Outline malaria parasites and classify them by life-cycle stage.
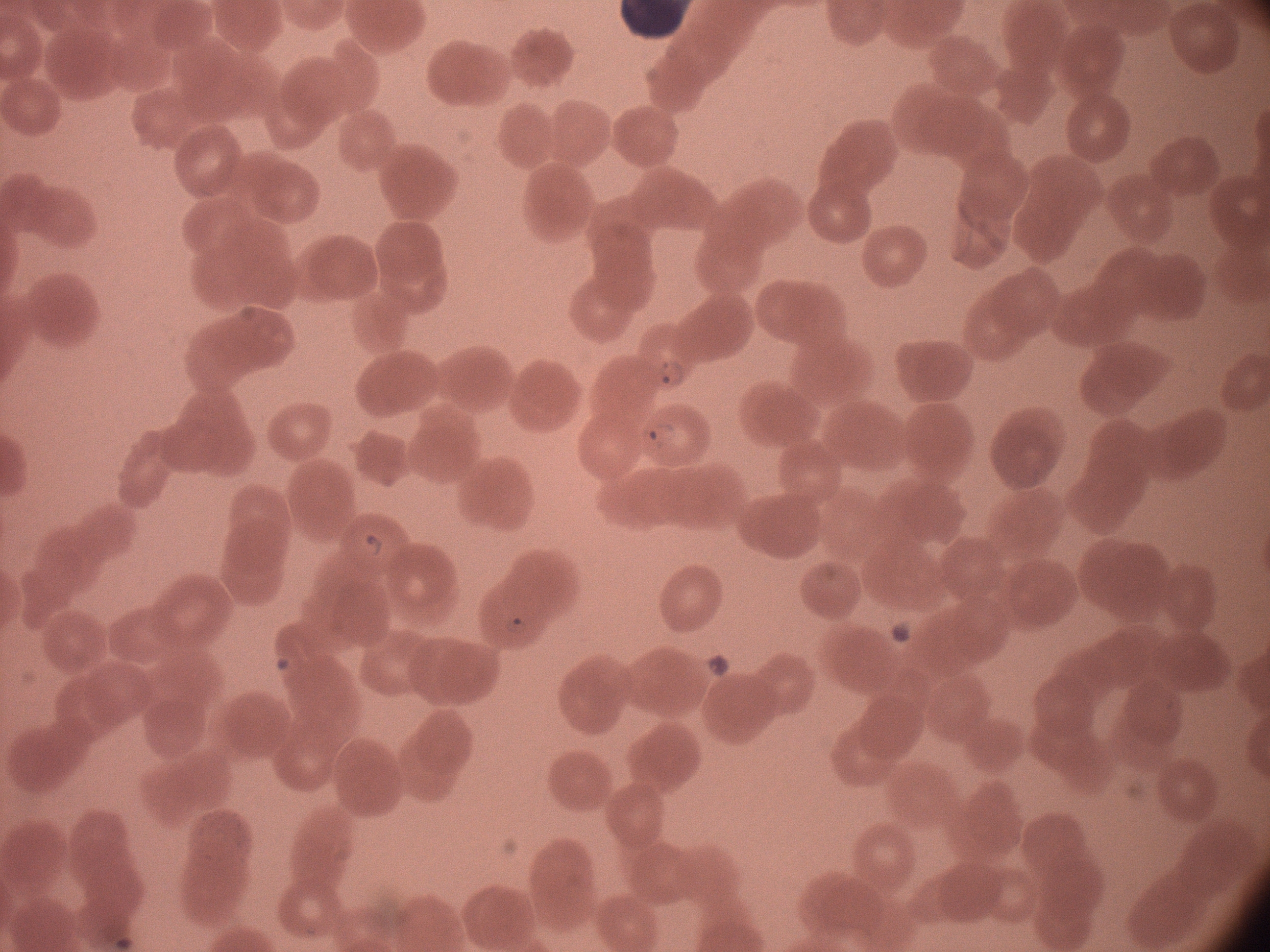

Approximate bounding boxes as (x1,y1)-(x2,y2) corner pairs in pixels, from the source annotation, which is not necessarily exhaustive.
Ring forms: (647,352)-(690,401), (636,416)-(685,453), (359,522)-(394,559), (494,601)-(532,642).

Species: Plasmodium falciparum. Image is 1270×952 pixels. Acquired with a Leica DM2000 optical microscope and its built-in camera. Single field of view. Giemsa-stained preparation. Captured at 100x magnification. Thin blood smear.